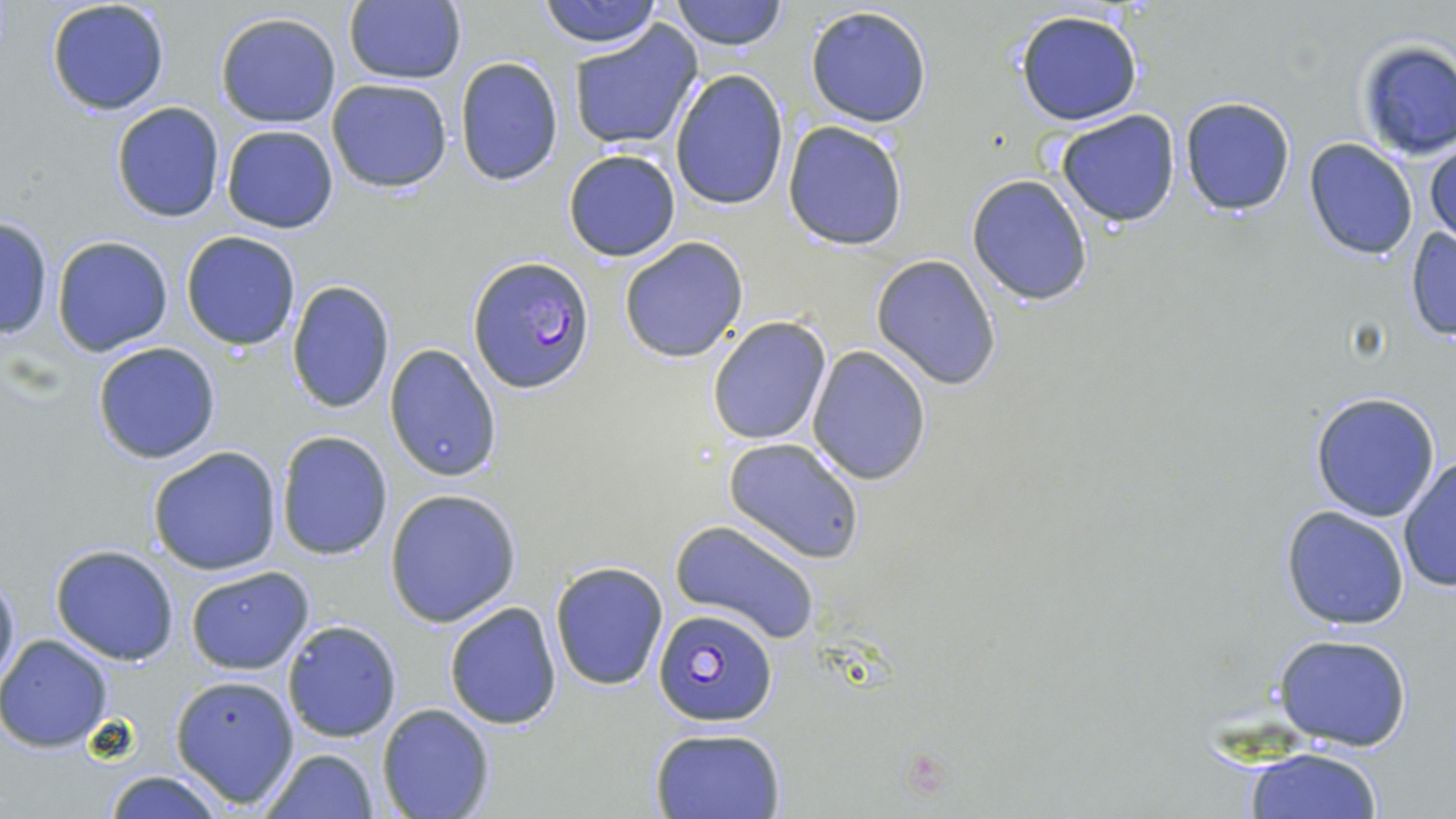 Approximate bounding boxes as (x1, y1, x2, y2) in pixels. Plasmodium falciparum-infected red blood cell locations: (469, 256, 594, 395), (653, 606, 779, 726). Uninfected red blood cell locations: (537, 0, 662, 48), (671, 0, 786, 50), (45, 1, 171, 117), (342, 1, 467, 84), (804, 5, 934, 129), (1014, 10, 1143, 126), (215, 12, 343, 128), (568, 19, 705, 154), (1353, 39, 1456, 159), (454, 55, 563, 187), (669, 68, 791, 212), (326, 78, 453, 193), (1178, 95, 1298, 217), (111, 101, 225, 222), (1056, 110, 1181, 226), (783, 120, 908, 250), (222, 125, 338, 234), (1302, 137, 1419, 260), (1425, 139, 1456, 251), (563, 148, 682, 262), (966, 174, 1094, 307), (0, 215, 54, 340), (1403, 226, 1455, 342), (181, 230, 302, 350), (51, 234, 174, 357), (618, 236, 749, 362), (871, 255, 1001, 390), (286, 279, 396, 414), (706, 315, 833, 446), (91, 341, 222, 464), (385, 344, 503, 482), (807, 346, 931, 485), (1309, 391, 1442, 522), (275, 430, 394, 561), (723, 437, 866, 564), (147, 447, 282, 575), (1399, 455, 1456, 593), (385, 489, 521, 627), (1279, 505, 1411, 630), (669, 520, 820, 647), (49, 545, 181, 665), (551, 562, 669, 689), (184, 565, 314, 675), (1, 568, 20, 691), (443, 601, 562, 731), (282, 619, 401, 744), (0, 634, 115, 752), (1274, 635, 1414, 751), (170, 673, 299, 808), (377, 703, 494, 819), (649, 726, 786, 818), (1241, 746, 1384, 819), (259, 747, 379, 819), (102, 770, 229, 819). Slide-level diagnosis: Plasmodium falciparum. One field of a larger specimen. 1000x magnification. May-Grünwald-Giemsa-stained preparation. Thin blood smear. Image is 1456×819 pixels. Optical microscopy.